Identify the parasite.
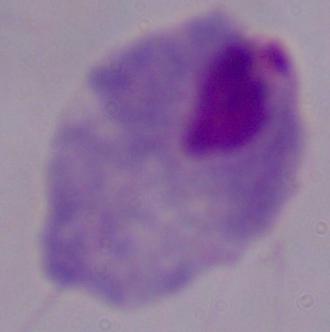

A trichomonad.

{
  "modality": "micrograph",
  "magnification": "1000x"
}